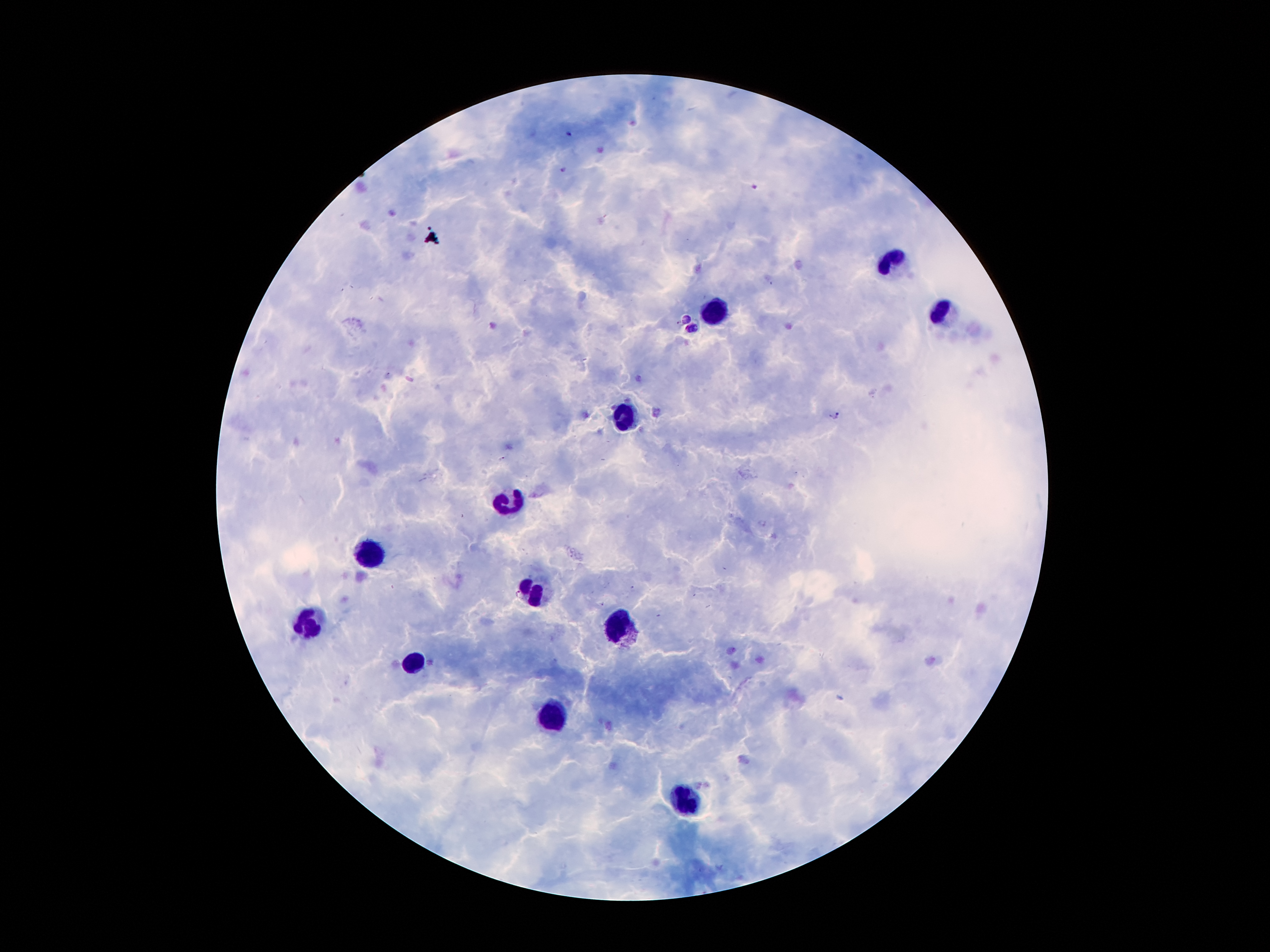

coordinate format = approximate centers as (x, y) in pixels
Plasmodium parasite locations = (570, 134), (563, 170), (753, 185), (685, 318), (692, 330), (836, 415)
leukocyte locations = (895, 263), (720, 309), (941, 316), (627, 414), (509, 508), (367, 551), (533, 587), (310, 621), (622, 630), (418, 661), (547, 719), (689, 801)
capture = smartphone camera through the microscope eyepiece
image size = 1270×952 pixels
preparation = thick peripheral-blood smear
patient malaria status = infected with Plasmodium falciparum
field of view = single
stain = Giemsa
magnification = 100x